Assess the morphology of the red blood cells.
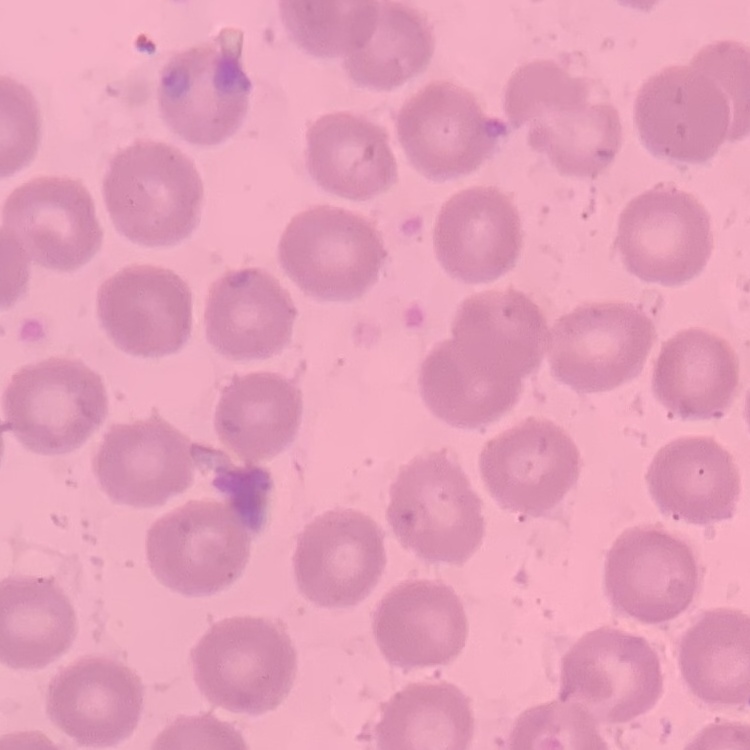

No rouleaux formation.

Field's or Giemsa stain. One tile cut from a larger photomicrograph. Thin blood smear.